Identify the parasite.
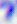
This is Toxoplasma gondii.

400x magnification. Photomicrograph.